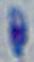
Toxoplasma gondii is shown. Captured at 1000x magnification. Micrograph.